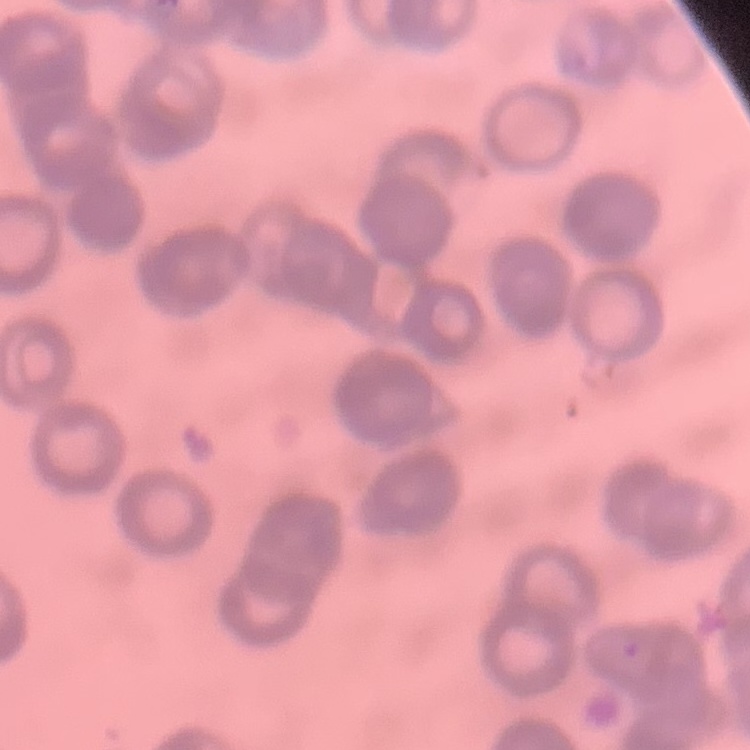
Summary:
  - Erythrocyte morphology: rouleaux formation
  - Image type: square crop of a larger photomicrograph
  - Stain: Field's or Giemsa
  - Preparation: thin peripheral smear